Assess this cell for malaria.
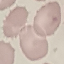

It is uninfected.

Acquired by smartphone through the microscope eyepiece. Thin blood film. Automatically extracted cell patch, resized to 64 × 64 pixels. Giemsa-stained preparation.